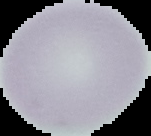

image_type: segmented cell region with the area outside set to black
result: no malaria parasites detected
preparation: thin blood film
image_size: 151×136 pixels